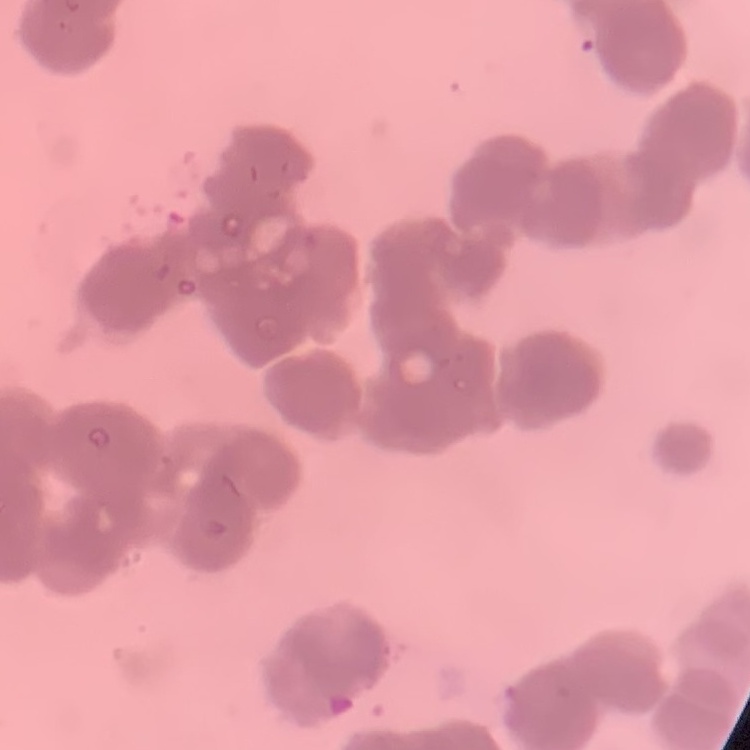
The red blood cells exhibit rouleaux formation. Square crop of a larger photomicrograph. Field's or Giemsa stain. Thin blood smear.